Report the malaria status of this cell.
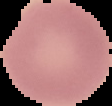
Uninfected.

{
  "preparation": "thin blood film",
  "image_type": "segmented cell region with the area outside set to black",
  "image_size": "112×106 pixels"
}